Give the position of every Plasmodium parasite visible.
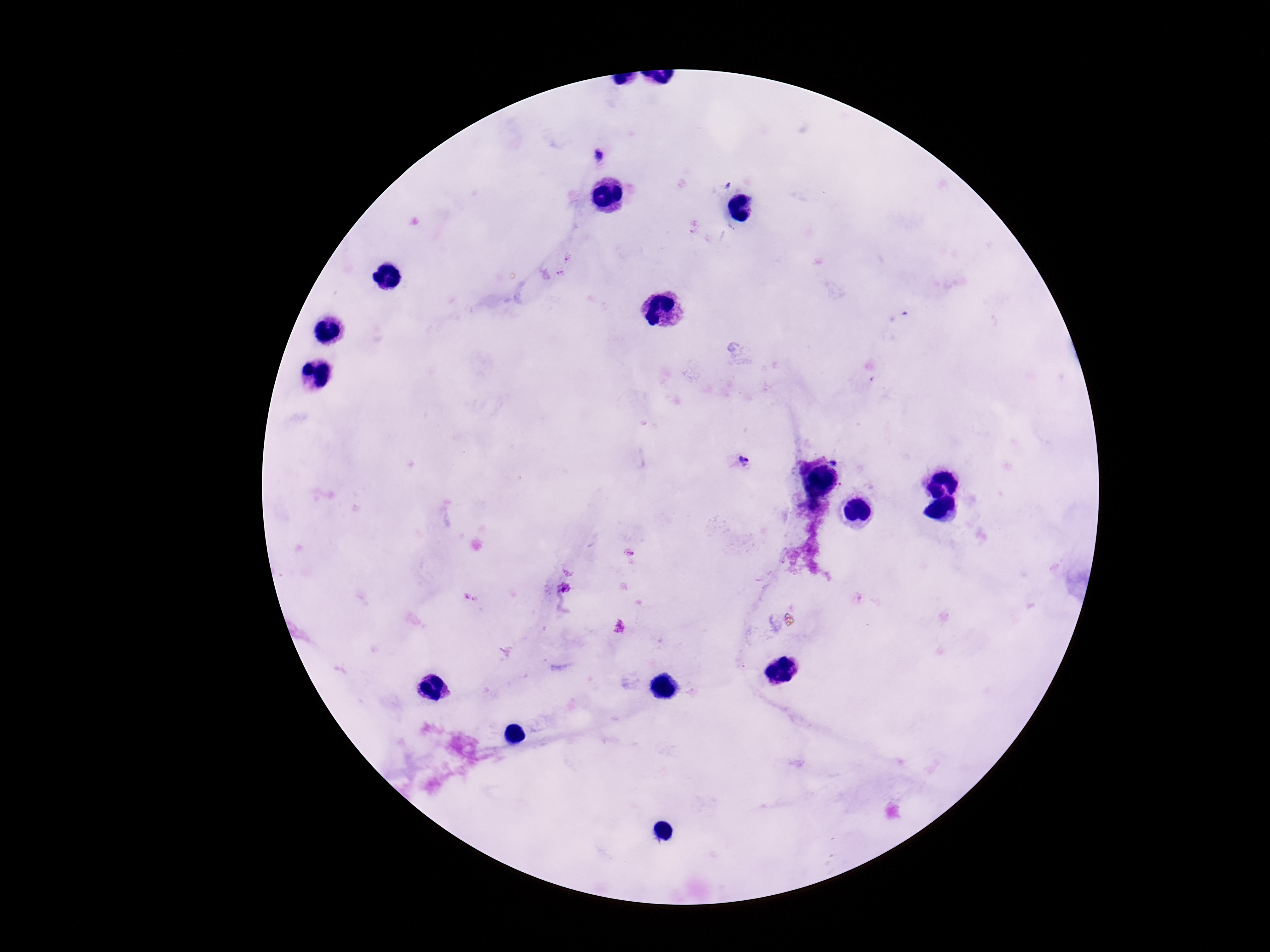
Approximate object centers, in pixels from the top-left corner.
Plasmodium parasites: (x=597, y=155), (x=898, y=315), (x=745, y=460).

Thick blood film. Patient malaria status: positive. Giemsa stain. 100x magnification. Image is 1270×952 pixels. One field from this slide. Photographed through the microscope eyepiece with a smartphone camera.